State the blood parasite species.
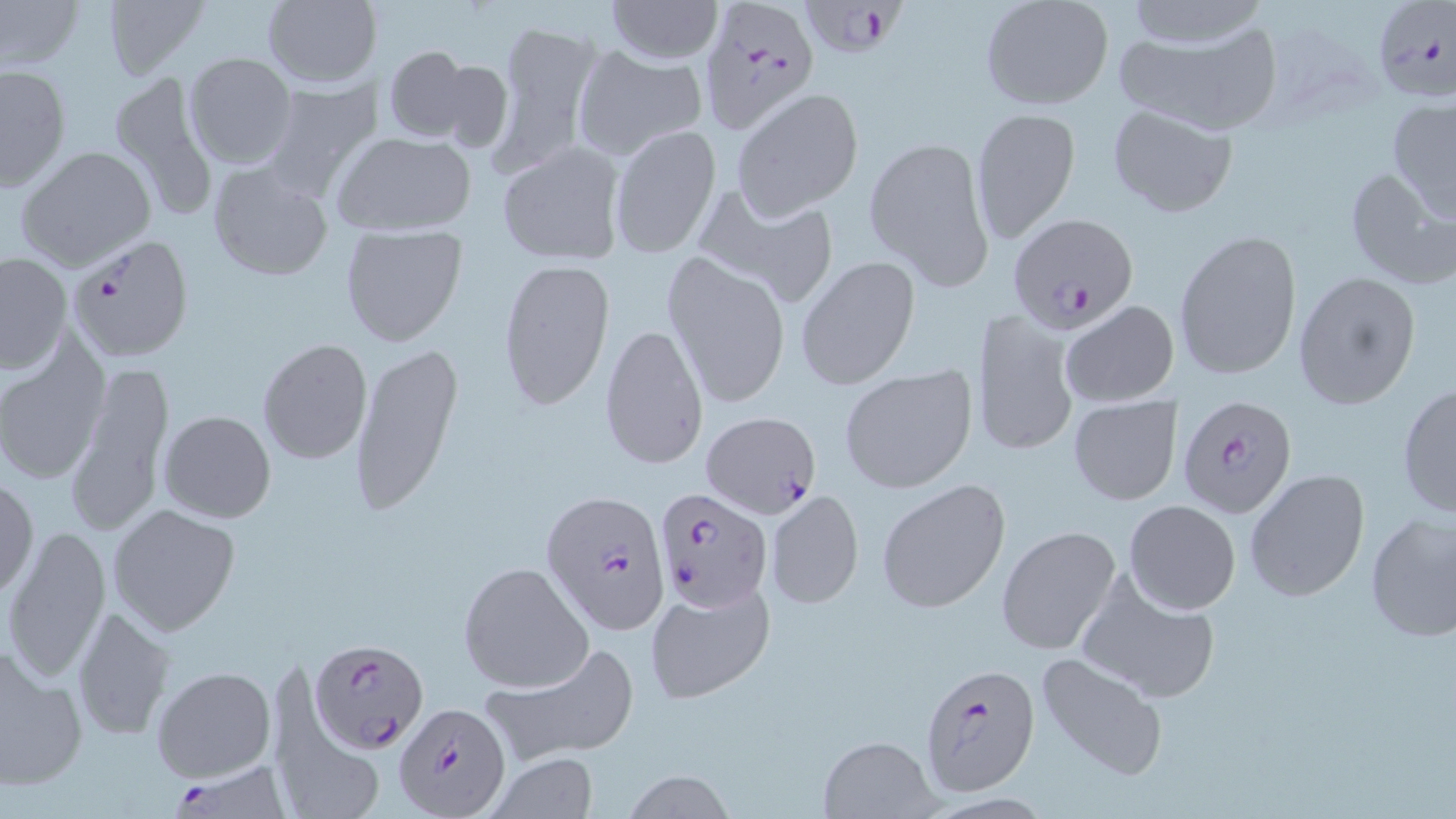

Plasmodium falciparum.

{
  "magnification": "1000x",
  "field_of_view": "single",
  "modality": "optical microscopy",
  "uninfected_red_blood_cell_locations": "approximate bounding boxes as (x1, y1, x2, y2) in pixels: (1, 0, 83, 72), (262, 0, 377, 90), (606, 0, 724, 63), (1119, 0, 1270, 50), (101, 1, 210, 80), (979, 2, 1113, 112), (489, 17, 602, 178), (1108, 26, 1279, 131), (382, 45, 480, 143), (575, 47, 706, 160), (183, 52, 297, 169), (1, 63, 70, 192), (107, 71, 221, 223), (259, 76, 380, 199), (733, 89, 863, 218), (1388, 97, 1456, 221), (1105, 102, 1239, 218), (972, 108, 1083, 244), (608, 128, 721, 256), (333, 131, 477, 237), (866, 135, 994, 289), (497, 139, 627, 264), (15, 145, 155, 271), (207, 162, 334, 280), (1340, 165, 1452, 290), (697, 185, 841, 309), (339, 225, 469, 348), (1174, 229, 1300, 381), (663, 252, 790, 410), (1, 254, 71, 374), (796, 257, 919, 390), (497, 259, 617, 410), (1292, 271, 1422, 410), (1061, 302, 1179, 407), (972, 308, 1078, 458), (599, 322, 709, 470), (257, 338, 373, 464), (0, 340, 108, 485), (349, 341, 464, 518), (67, 361, 173, 538), (839, 366, 977, 493), (1396, 381, 1456, 520), (1067, 396, 1179, 505), (159, 410, 276, 523), (1244, 468, 1371, 602), (1, 477, 38, 600), (877, 478, 1012, 615), (765, 489, 864, 609), (1124, 499, 1241, 614), (106, 503, 240, 635), (1363, 510, 1456, 643), (996, 525, 1121, 655), (3, 526, 112, 684), (458, 562, 593, 693), (1073, 569, 1222, 704), (645, 579, 775, 705), (70, 607, 175, 741), (480, 640, 639, 766), (0, 642, 88, 793), (1035, 653, 1169, 782), (268, 657, 382, 819), (152, 664, 275, 781), (815, 733, 943, 818), (485, 753, 600, 818), (624, 772, 736, 818)",
  "plasmodium_falciparum_infected_red_blood_cell_locations": "approximate bounding boxes as (x1, y1, x2, y2) in pixels: (802, 0, 904, 54), (1371, 0, 1455, 106), (701, 2, 816, 133), (1009, 212, 1138, 333), (67, 232, 194, 361), (1177, 395, 1297, 517), (701, 412, 820, 518), (652, 487, 771, 613), (543, 491, 666, 634), (310, 639, 429, 752), (918, 663, 1042, 795), (393, 703, 513, 817), (167, 762, 293, 815)",
  "stain": "May-Grünwald-Giemsa",
  "image_size": "1456×819 pixels",
  "preparation": "thin blood film"
}